Report the malaria status of this cell.
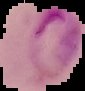

It is parasitized.

image_size: 85×91 pixels
image_type: segmented cell region on a black background
preparation: thin blood smear